Report the malaria status of this cell.
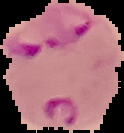
Parasitized.

Image is 124×133 pixels. From a thin blood smear. Cell region segmented out of the field of view; the surrounding area is masked to black.